Point out each Plasmodium parasite and each leukocyte.
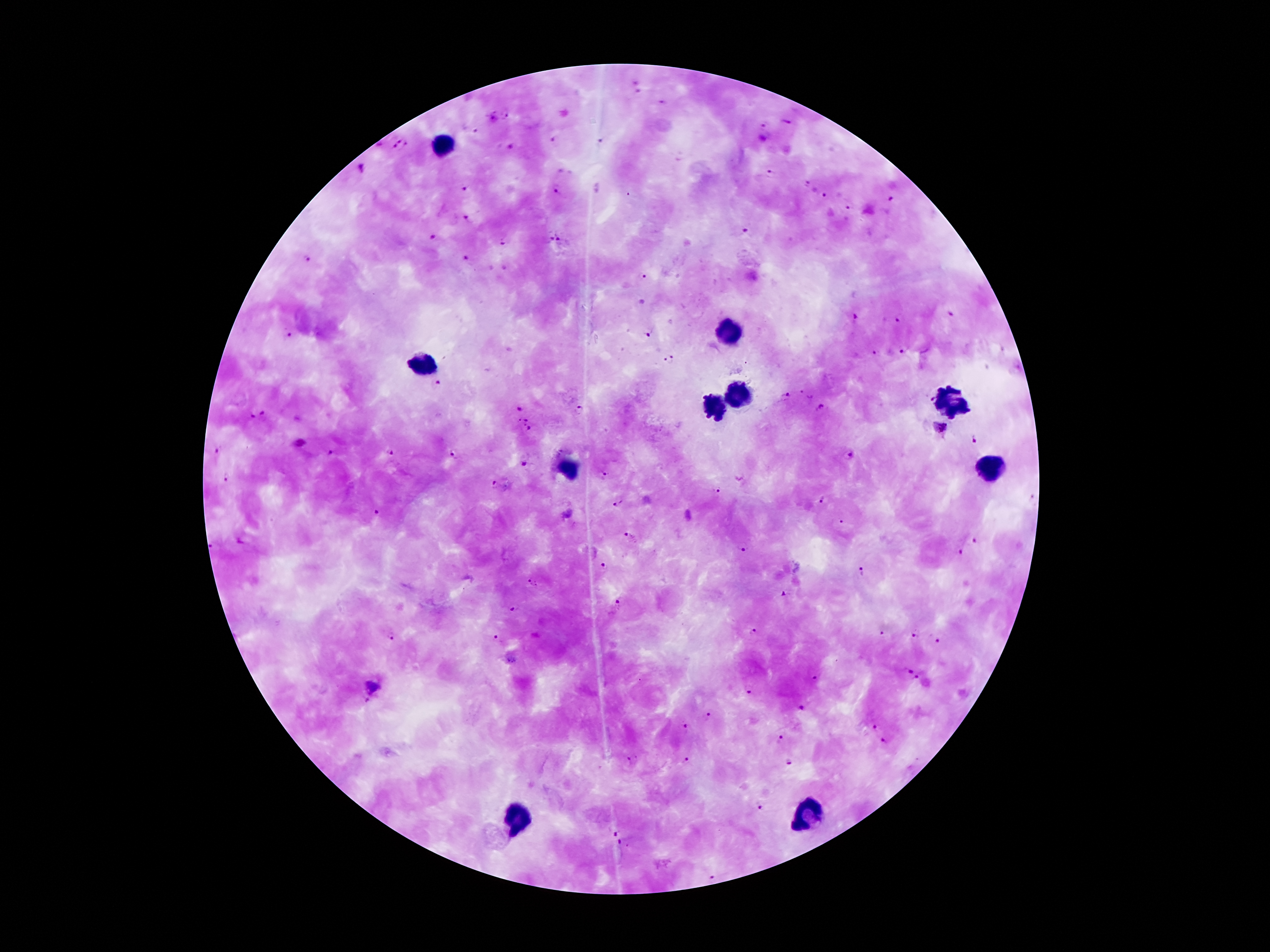
Approximate centers as {x, y} in pixels.
Plasmodium parasites: {636, 80}, {638, 94}, {664, 102}, {507, 114}, {491, 117}, {785, 122}, {764, 125}, {475, 132}, {553, 140}, {601, 141}, {378, 144}, {400, 145}, {510, 147}, {359, 169}, {771, 173}, {807, 183}, {463, 187}, {558, 193}, {630, 196}, {824, 196}, {891, 200}, {848, 207}, {469, 217}, {745, 231}, {435, 235}, {547, 240}, {504, 241}, {562, 242}, {467, 257}, {307, 260}, {642, 277}, {949, 314}, {853, 316}, {900, 318}, {647, 335}, {289, 336}, {902, 351}, {877, 352}, {668, 361}, {436, 383}, {789, 395}, {930, 399}, {578, 407}, {820, 407}, {519, 409}, {264, 414}, {254, 419}, {525, 419}, {941, 427}, {530, 429}, {974, 440}, {300, 442}, {217, 450}, {391, 451}, {330, 452}, {457, 453}, {847, 455}, {525, 465}, {609, 475}, {226, 477}, {495, 485}, {716, 492}, {1035, 500}, {823, 501}, {617, 503}, {376, 513}, {842, 522}, {627, 536}, {974, 540}, {212, 544}, {743, 550}, {960, 553}, {603, 565}, {862, 574}, {533, 582}, {784, 594}, {619, 601}, {511, 609}, {753, 633}, {880, 633}, {916, 636}, {391, 637}, {497, 638}, {939, 641}, {908, 670}, {816, 679}, {916, 679}, {748, 689}, {368, 701}, {800, 707}, {708, 716}, {875, 728}, {685, 730}, {780, 739}, {884, 742}, {632, 758}, {686, 761}, {789, 762}, {759, 808}, {617, 833}, {620, 843}, {712, 878}.
Leukocytes: {447, 143}, {726, 334}, {424, 361}, {733, 393}, {946, 402}, {715, 406}, {567, 468}, {989, 468}, {808, 815}, {513, 819}.

Patient malaria status: infected with Plasmodium falciparum. Image is 1270×952 pixels. Single field of view. Photographed through the microscope eyepiece with a smartphone camera. Thick peripheral-blood smear. Giemsa-stained preparation. 100x magnification.